Describe the morphology of the erythrocytes.
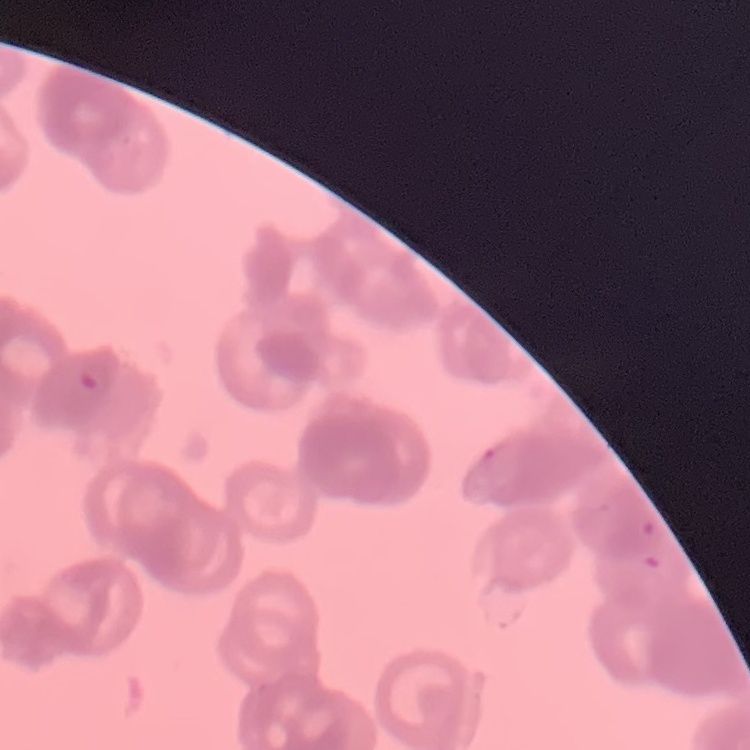

Rouleaux formation.

{
  "preparation": "thin blood film",
  "stain": "Field's or Giemsa",
  "image_type": "one tile cut from a larger photomicrograph"
}